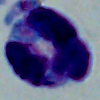

Summary:
  - Modality: photomicrograph
  - Magnification: 1000x
  - Identification: white blood cell